Locate every malaria parasite.
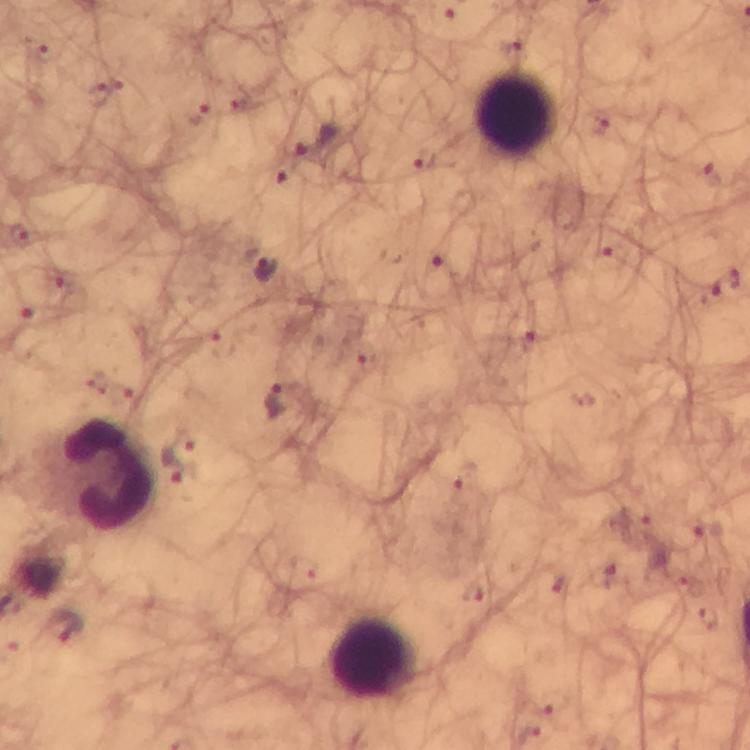
Approximate centers as [x, y] in pixels.
Malaria parasites: [99, 93], [316, 143], [425, 160], [712, 174], [19, 236], [618, 253], [443, 261], [263, 267], [725, 284], [30, 318], [530, 340], [278, 402], [178, 452], [636, 521], [705, 533], [474, 596], [64, 625].

Leukocyte locations: [517, 113], [109, 475], [374, 659]. Cropped region of a single field of view. 100x magnification. Immersion oil was used. From a diagnostic examination for malaria. Smartphone photograph taken through a microscope. Thick blood smear. Image is 750×750 pixels. Giemsa-stained preparation.